Look for Plasmodium parasites.
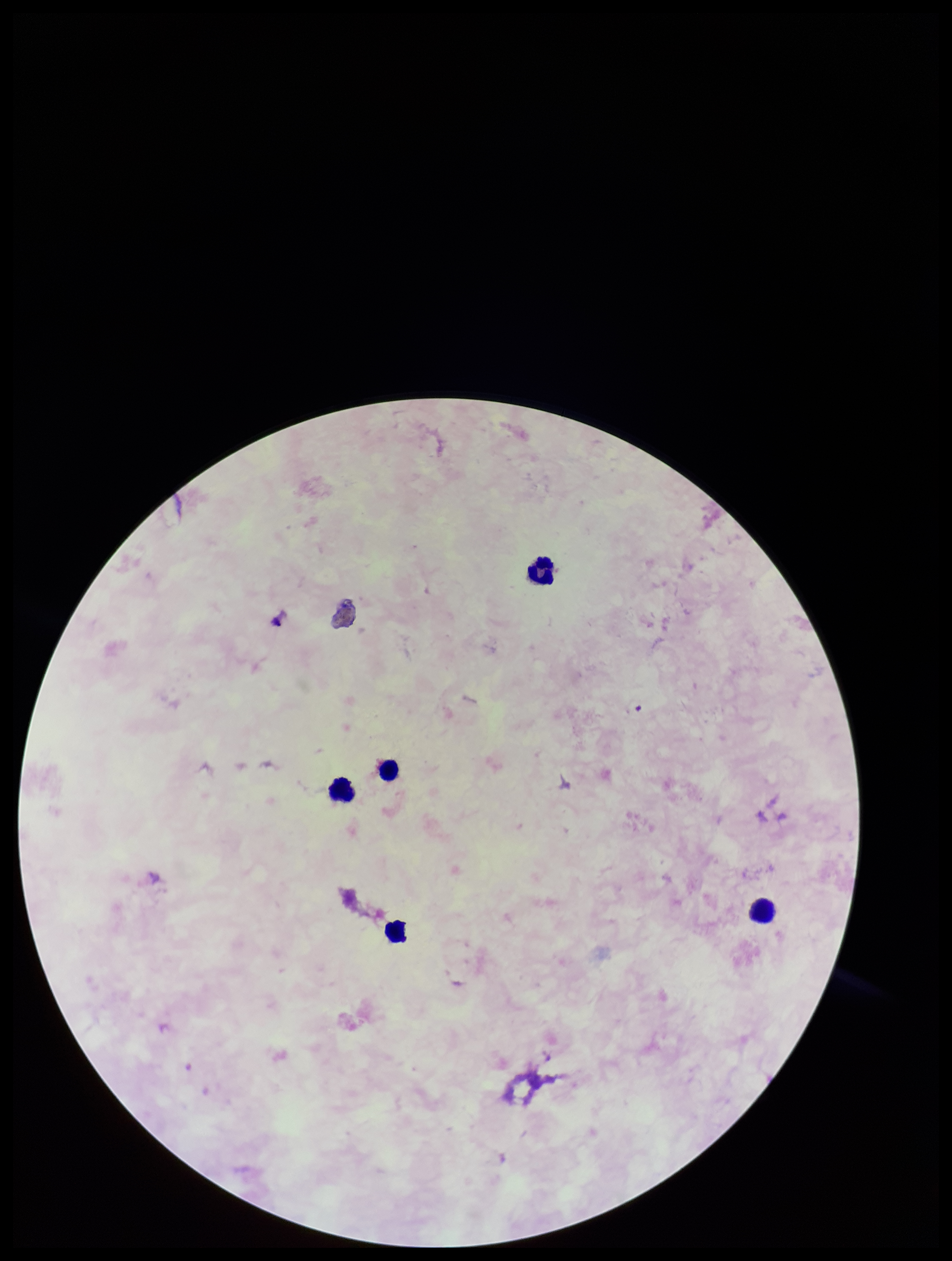
None detected.

Leukocyte count: 5. Preparation: thick smear. Photographed through the microscope eyepiece with a smartphone camera. Parasite count: 0. One field from this slide. Patient malaria status: negative. Image is 952×1261 pixels. Stained with Giemsa.